Give the extent of all Plasmodium falciparum-infected red blood cells.
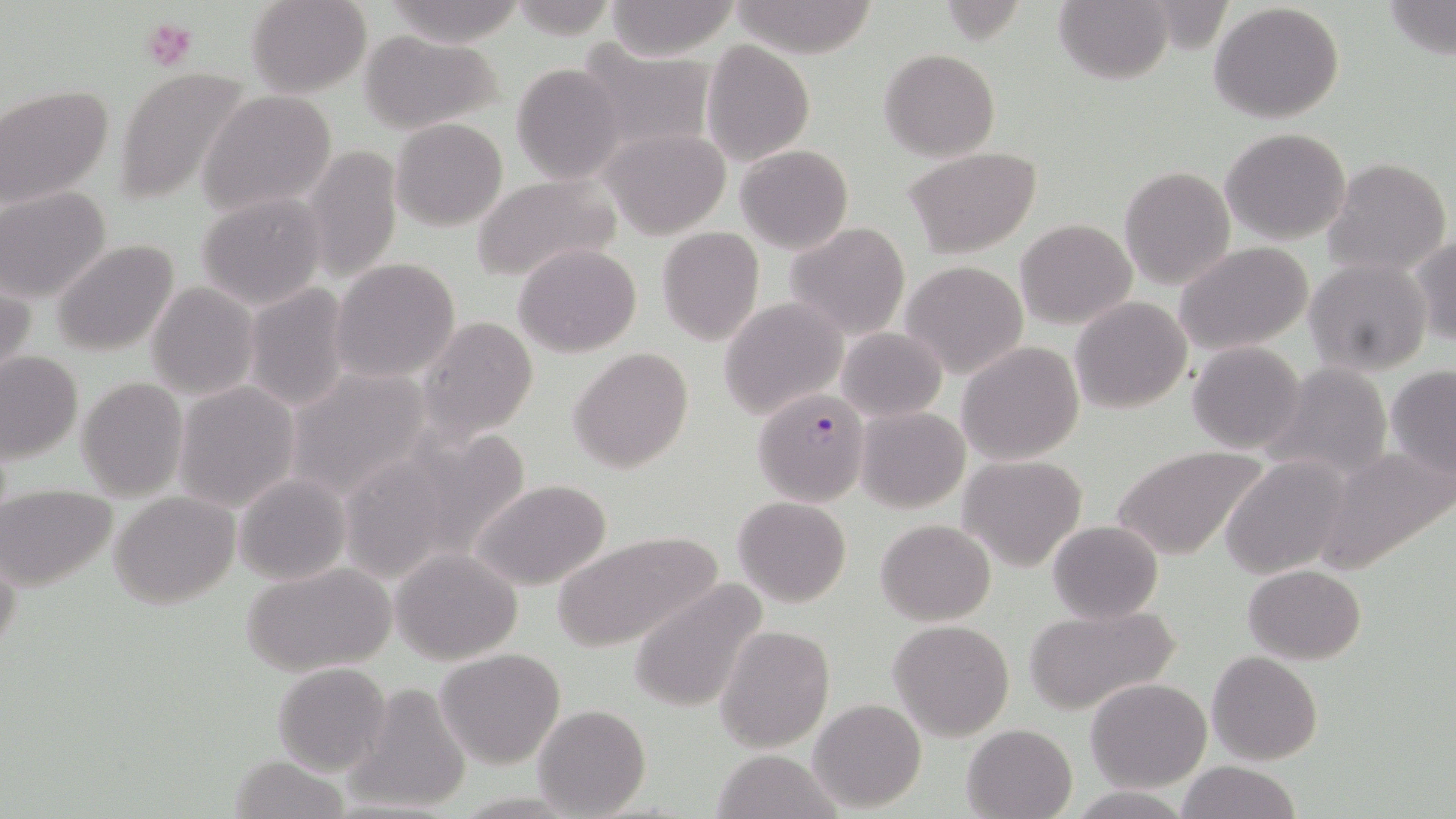
Approximate bounding boxes as [x1, y1, x2, y2] in pixels.
Plasmodium falciparum-infected red blood cells: [754, 387, 869, 505].

Summary:
  - Uninfected red blood cell locations: [246, 0, 371, 98], [383, 0, 525, 45], [729, 1, 879, 59], [1054, 1, 1172, 84], [1383, 1, 1455, 59], [604, 2, 739, 60], [1209, 2, 1346, 123], [357, 29, 504, 134], [702, 40, 815, 167], [576, 45, 715, 157], [880, 49, 1001, 161], [511, 63, 626, 184], [112, 68, 255, 207], [0, 84, 117, 210], [197, 90, 338, 216], [390, 118, 508, 232], [603, 126, 729, 238], [1220, 127, 1351, 245], [303, 142, 402, 287], [737, 145, 853, 253], [904, 146, 1042, 256], [1323, 157, 1452, 278], [1120, 166, 1234, 289], [469, 174, 622, 285], [0, 186, 112, 302], [196, 193, 327, 311], [1016, 218, 1137, 329], [783, 221, 911, 339], [657, 227, 766, 346], [1410, 234, 1456, 347], [50, 239, 182, 357], [1174, 240, 1317, 355], [513, 242, 642, 356], [330, 258, 461, 384], [1305, 258, 1432, 376], [901, 260, 1028, 379], [0, 276, 35, 391], [145, 282, 259, 399], [243, 285, 352, 412], [1070, 296, 1193, 415], [719, 298, 847, 419], [416, 315, 540, 444], [836, 327, 948, 422], [956, 340, 1083, 466], [1187, 342, 1307, 453], [568, 347, 694, 474], [0, 351, 83, 464], [1261, 361, 1393, 482], [1384, 365, 1456, 478], [286, 367, 432, 503], [77, 376, 187, 501], [173, 381, 300, 512], [855, 406, 969, 513], [1110, 444, 1269, 561], [1318, 445, 1455, 572], [959, 454, 1088, 571], [1220, 454, 1351, 580], [233, 471, 352, 586], [467, 477, 614, 592], [3, 486, 117, 591], [108, 491, 241, 608], [734, 495, 852, 607], [876, 519, 995, 625], [1046, 519, 1163, 623], [551, 531, 723, 652], [0, 541, 20, 671], [391, 547, 522, 665], [242, 562, 397, 677], [1244, 565, 1367, 663], [629, 577, 769, 716], [1024, 604, 1181, 716], [889, 620, 1015, 740], [715, 624, 834, 751], [436, 648, 565, 768], [1207, 651, 1323, 764], [272, 662, 392, 778], [353, 666, 562, 792], [1084, 677, 1211, 791], [348, 683, 472, 814], [808, 697, 927, 810], [534, 704, 650, 816], [962, 723, 1078, 818], [710, 749, 840, 818], [229, 754, 349, 819], [1176, 762, 1301, 819]
  - Platelet locations: [140, 15, 197, 74]
  - Slide-level diagnosis: Plasmodium falciparum
  - Field of view: single
  - Magnification: 1000x
  - Preparation: thin blood film
  - Image size: 1456×819 pixels
  - Stain: May-Grünwald-Giemsa
  - Modality: light microscopy